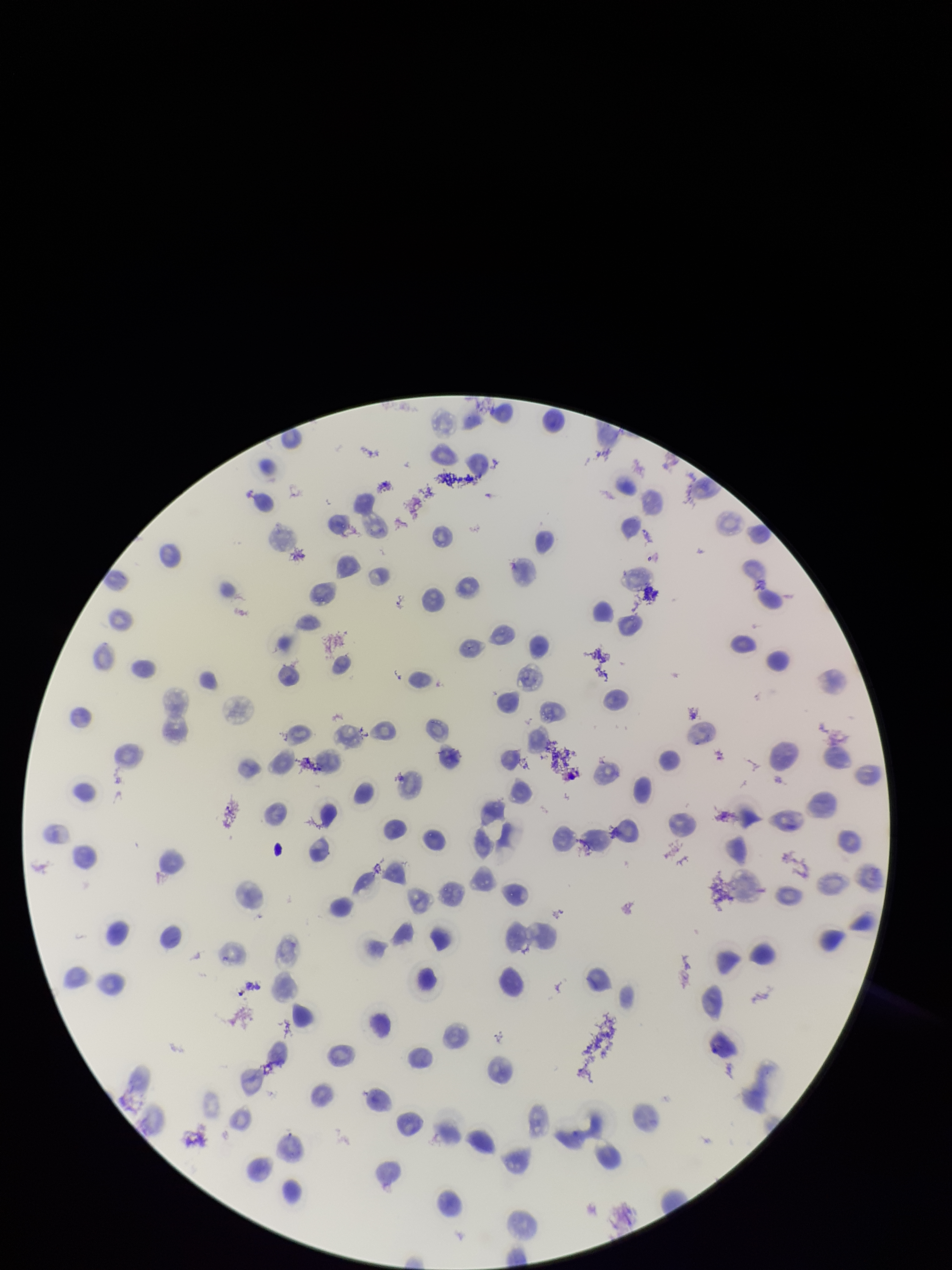
Photographed through the microscope eyepiece with a smartphone camera. Red blood cell count: 115. Giemsa stain. Parasitized red blood cell count: 0. Patient malaria status: positive. Parasitized red blood cells: none seen. Preparation: thin. Species reported for this patient: Plasmodium vivax. Single field of view. Image is 952×1270 pixels.